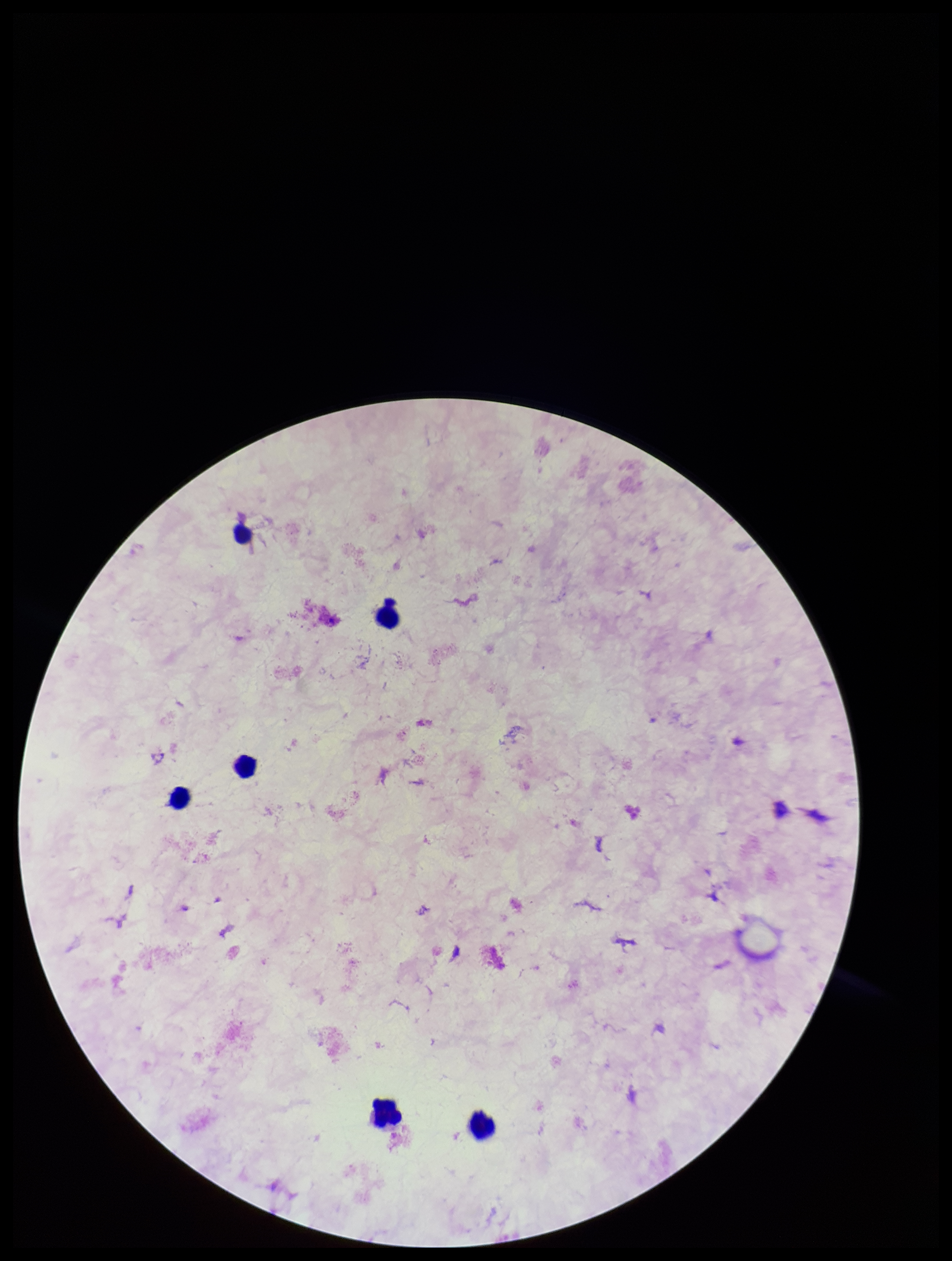

Summary:
  - Preparation: thick
  - Image size: 952×1261 pixels
  - Parasite count: 0
  - Patient malaria status: negative
  - Capture: smartphone photograph through the microscope eyepiece
  - Stain: Giemsa
  - Plasmodium parasites: none detected
  - Leukocyte count: 6
  - Field of view: one from this slide